Outline every parasitised red blood cell.
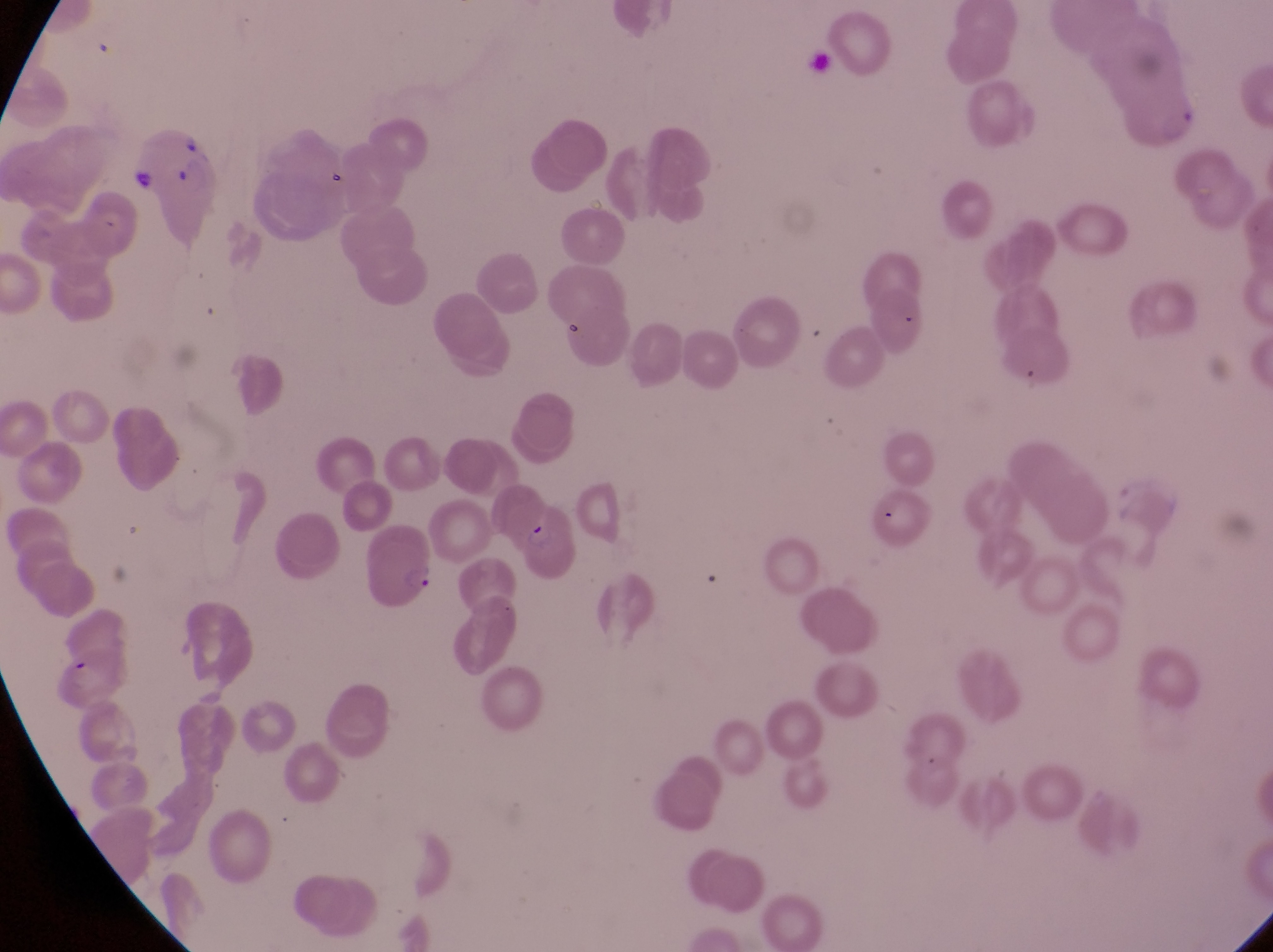

Approximate bounding boxes as [left, top, right, bottom] in pixels.
Parasitised red blood cells: [502, 505, 582, 582], [360, 529, 438, 617].

{
  "image_size": "1273×952 pixels",
  "country": "Uganda",
  "trophozoite_locations": "approximate bounding boxes as [left, top, right, bottom] in pixels: [1158, 97, 1201, 142], [132, 164, 157, 197]",
  "capture": "smartphone photograph through the eyepiece of an Olympus CX-23 microscope",
  "preparation": "thin blood smear",
  "magnification": "1000x",
  "field_of_view": "single"
}